Point out each leukocyte.
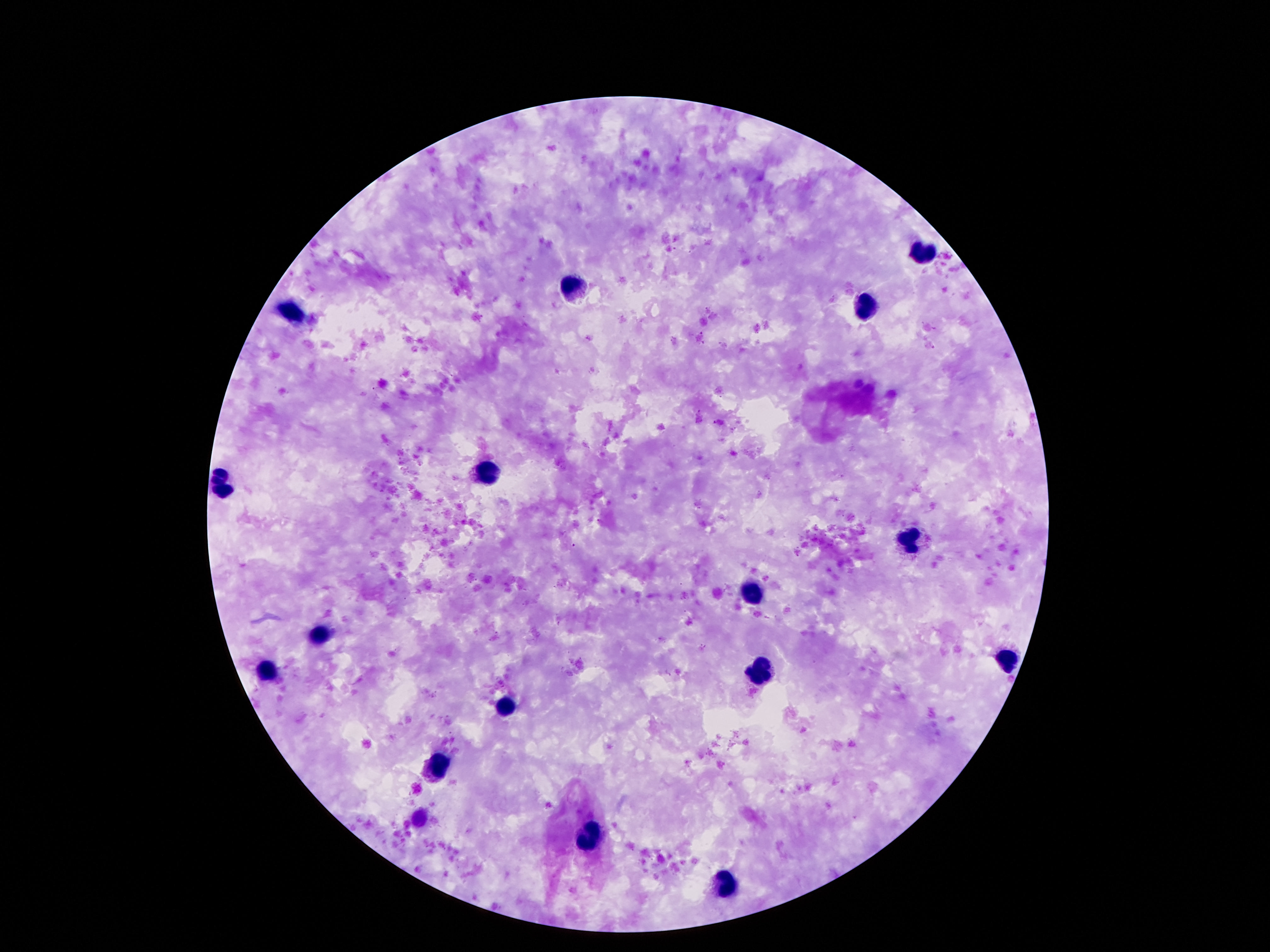
Approximate centers as (x, y) in pixels.
Leukocytes: (920, 251), (569, 288), (870, 307), (290, 314), (486, 474), (221, 484), (909, 537), (750, 593), (318, 637), (1006, 656), (760, 668), (267, 671), (506, 706), (439, 769), (591, 838), (723, 888).

Single field of view. Patient malaria status: uninfected. Image is 1270×952 pixels. Thick blood film. Smartphone photograph taken through the microscope eyepiece. Giemsa stain. 100x magnification.